Name the blood parasite species.
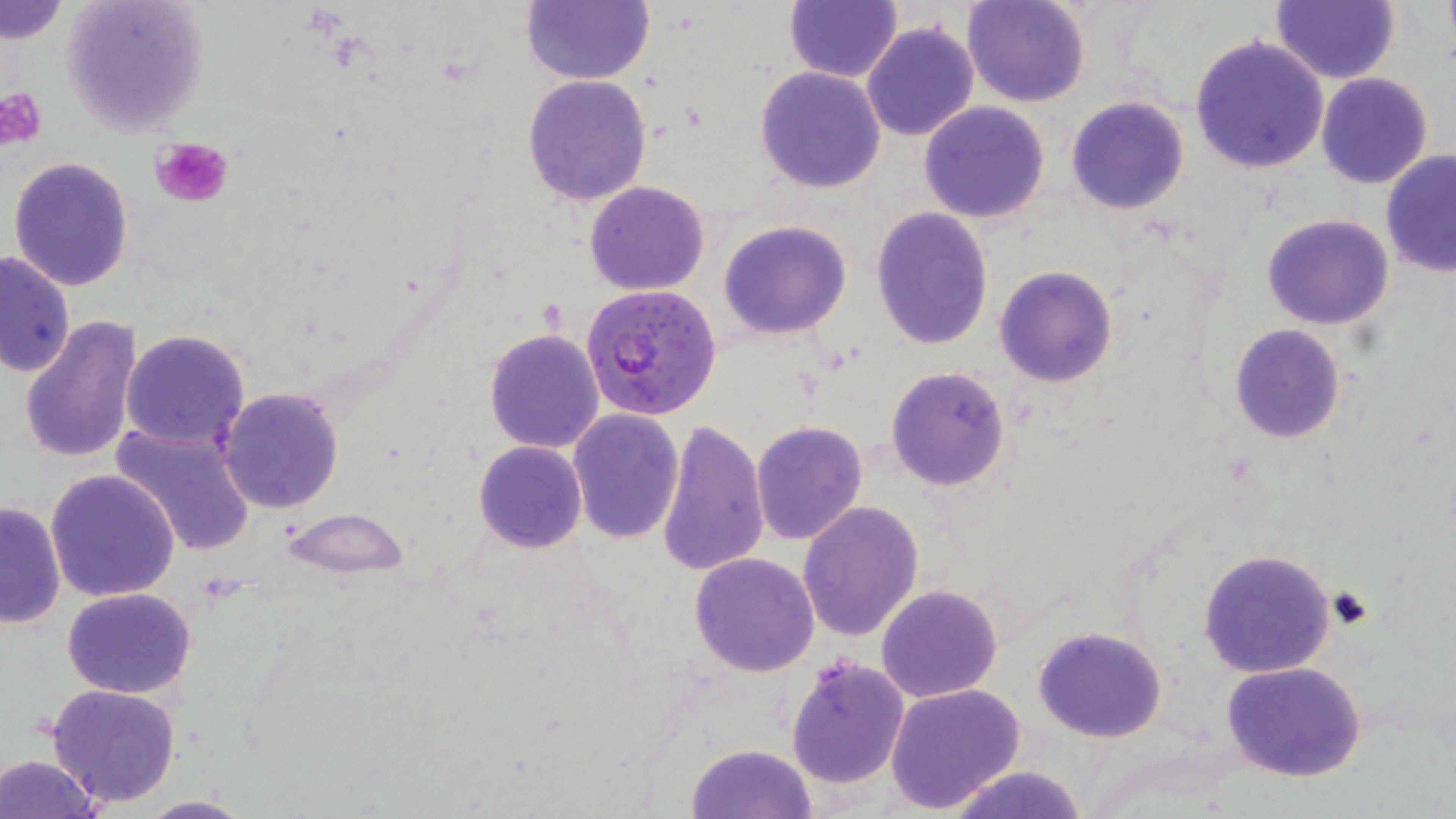
Plasmodium falciparum.

Approximate bounding boxes as (x1,y1)-(x2,y2) corner pairs in pixels. Uninfected red blood cell locations: (59,0)-(209,138), (522,0)-(655,85), (964,0)-(1091,107), (1272,0)-(1398,84), (1,1)-(68,43), (785,1)-(901,82), (861,21)-(980,141), (1188,34)-(1331,174), (756,65)-(887,193), (1315,72)-(1434,189), (522,74)-(652,208), (1065,95)-(1191,216), (919,101)-(1051,224), (1380,151)-(1456,277), (7,155)-(134,291), (585,180)-(710,295), (870,210)-(994,350), (1262,214)-(1394,329), (719,220)-(851,340), (0,249)-(75,379), (995,266)-(1118,388), (20,315)-(144,467), (1229,324)-(1346,443), (483,328)-(605,454), (119,329)-(251,451), (886,365)-(1011,492), (217,386)-(345,514), (567,409)-(685,544), (657,417)-(769,578), (751,420)-(868,546), (109,423)-(257,558), (473,440)-(588,554), (45,469)-(180,603), (0,500)-(66,629), (797,502)-(924,642), (279,507)-(409,579), (1196,549)-(1337,678), (688,552)-(820,676), (877,583)-(1003,701), (62,586)-(196,698), (1033,625)-(1169,743), (786,656)-(909,793), (1221,661)-(1368,782), (47,683)-(182,807), (885,683)-(1027,813), (687,742)-(816,818), (0,754)-(101,819), (943,765)-(1092,819), (134,794)-(256,817). Platelet locations: (1,88)-(49,150), (150,135)-(233,209). Plasmodium falciparum-infected red blood cell locations: (582,281)-(723,419). Optical microscopy. Single field of view. Thin blood smear. Captured at 1000x magnification. Image is 1456×819 pixels. May-Grünwald-Giemsa-stained preparation.